Identify the cell.
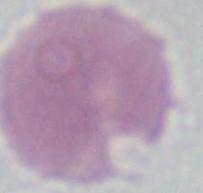

This is an erythrocyte.

Micrograph. 1000x magnification.